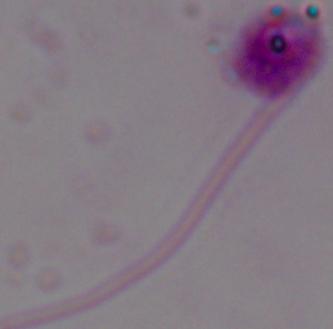
modality = micrograph
magnification = 1000x
identification = Leishmania